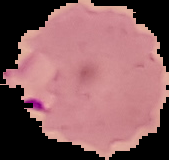

result = malaria parasites detected
image type = segmented cell region with the area outside set to black
preparation = thin blood smear
image size = 169×160 pixels